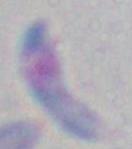 Toxoplasma gondii is seen. 1000x magnification. Micrograph.